Locate every blood parasite and identify its species.
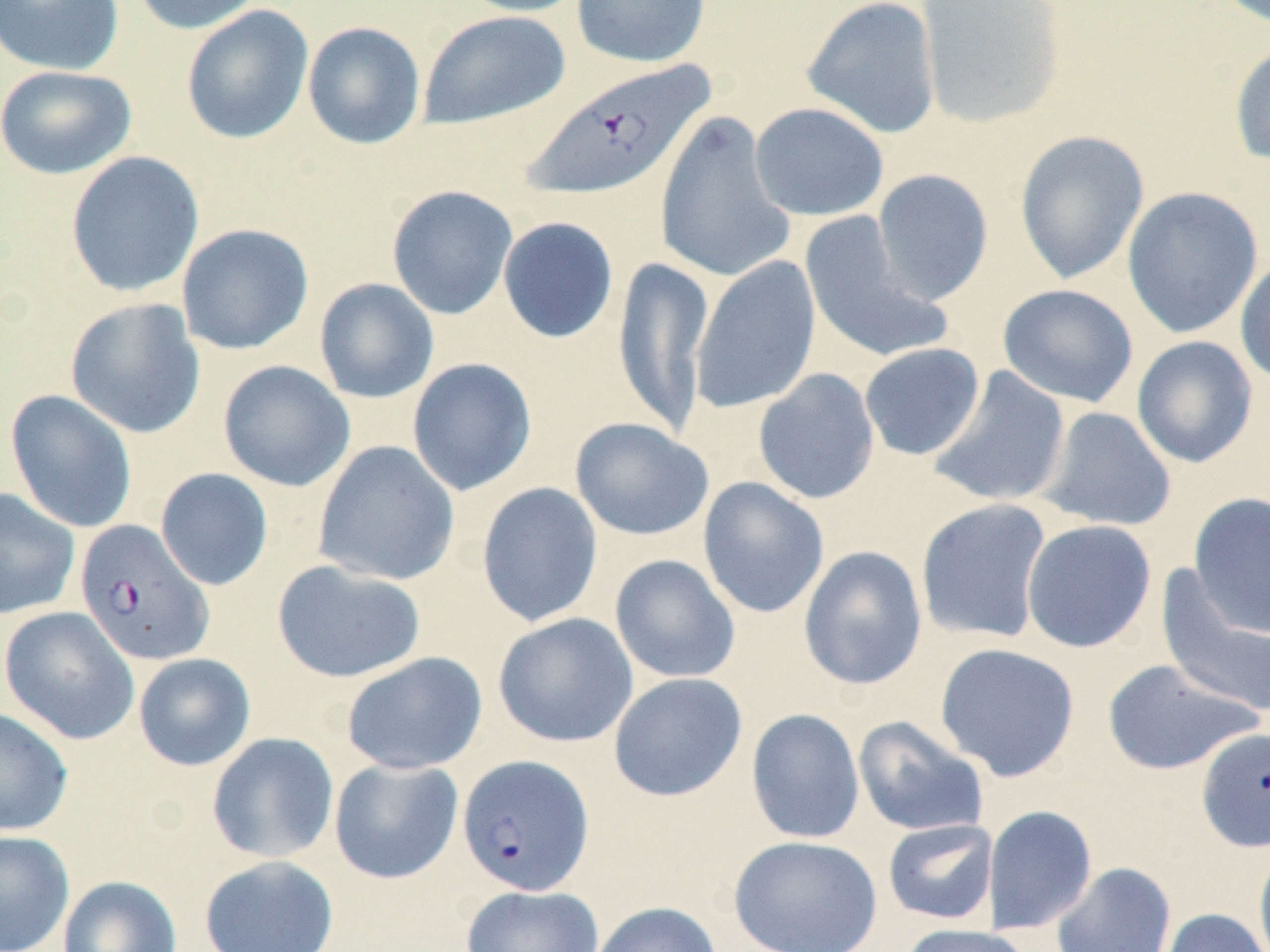
Approximate bounding boxes as (x1,y1)-(x2,y2) corner pairs in pixels.
Plasmodium falciparum-infected red blood cells (subset): (521,59)-(717,202), (75,520)-(214,666), (457,754)-(595,897).
No Plasmodium ovale, Plasmodium malariae, Plasmodium vivax, Babesia divergens, or Trypanosoma brucei observed.

{
  "slide_level_diagnosis": "Plasmodium falciparum",
  "stain": "May-Grünwald-Giemsa",
  "magnification": "1000x",
  "image_size": "1270×952 pixels",
  "field_of_view": "single",
  "modality": "light microscopy",
  "preparation": "thin blood film",
  "uninfected_red_blood_cell_locations_subset": "approximate bounding boxes as (x1,y1)-(x2,y2) corner pairs in pixels: (0,0)-(125,76), (129,0)-(268,35), (453,0)-(590,17), (571,0)-(711,68), (801,0)-(942,139), (915,0)-(1067,130), (181,5)-(314,145), (416,10)-(571,131), (302,21)-(426,150), (1228,36)-(1270,165), (0,65)-(137,179), (749,102)-(889,221), (654,111)-(795,285), (1014,130)-(1149,285), (65,151)-(204,298), (872,169)-(994,305), (386,185)-(519,320), (1121,186)-(1264,339), (798,213)-(953,365), (497,216)-(619,344), (176,223)-(314,355), (1235,253)-(1270,387), (691,255)-(821,415), (612,256)-(715,436), (313,278)-(440,404), (997,284)-(1139,408), (64,298)-(206,439), (1131,335)-(1259,468), (859,343)-(986,461), (406,357)-(537,497), (218,360)-(356,492), (927,365)-(1071,508), (753,368)-(880,505), (5,389)-(138,534), (1038,406)-(1176,532), (569,417)-(714,541), (313,441)-(460,586), (155,467)-(274,591), (697,476)-(829,619), (476,482)-(603,628), (0,488)-(80,621), (1189,491)-(1270,637), (916,498)-(1053,643), (1020,519)-(1157,653), (798,545)-(928,691), (609,554)-(741,684), (271,560)-(427,684), (1156,566)-(1270,718), (1,606)-(140,745), (493,613)-(638,748), (934,642)-(1080,782), (341,651)-(488,775), (133,653)-(256,771), (1100,658)-(1263,776), (608,672)-(748,802), (0,707)-(73,837), (746,708)-(865,845), (852,716)-(989,837), (206,732)-(339,863), (329,758)-(464,884), (983,804)-(1098,934), (882,819)-(998,925), (0,830)-(75,952), (728,834)-(883,952), (1254,844)-(1270,952), (199,855)-(340,952), (1051,861)-(1176,952), (58,875)-(182,952), (460,884)-(604,952), (589,901)-(722,952), (1158,907)-(1269,952), (900,923)-(1034,952)"
}